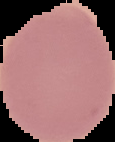
image type = cell region segmented out of the field of view; surrounding area masked to black
preparation = thin blood smear
image size = 115×142 pixels
malaria status = uninfected